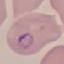 Result: malaria parasites identified. Photographed with a smartphone camera at the microscope eyepiece. Automatically extracted cell patch, resized to 64 × 64 pixels. Thin blood film. Giemsa stain.